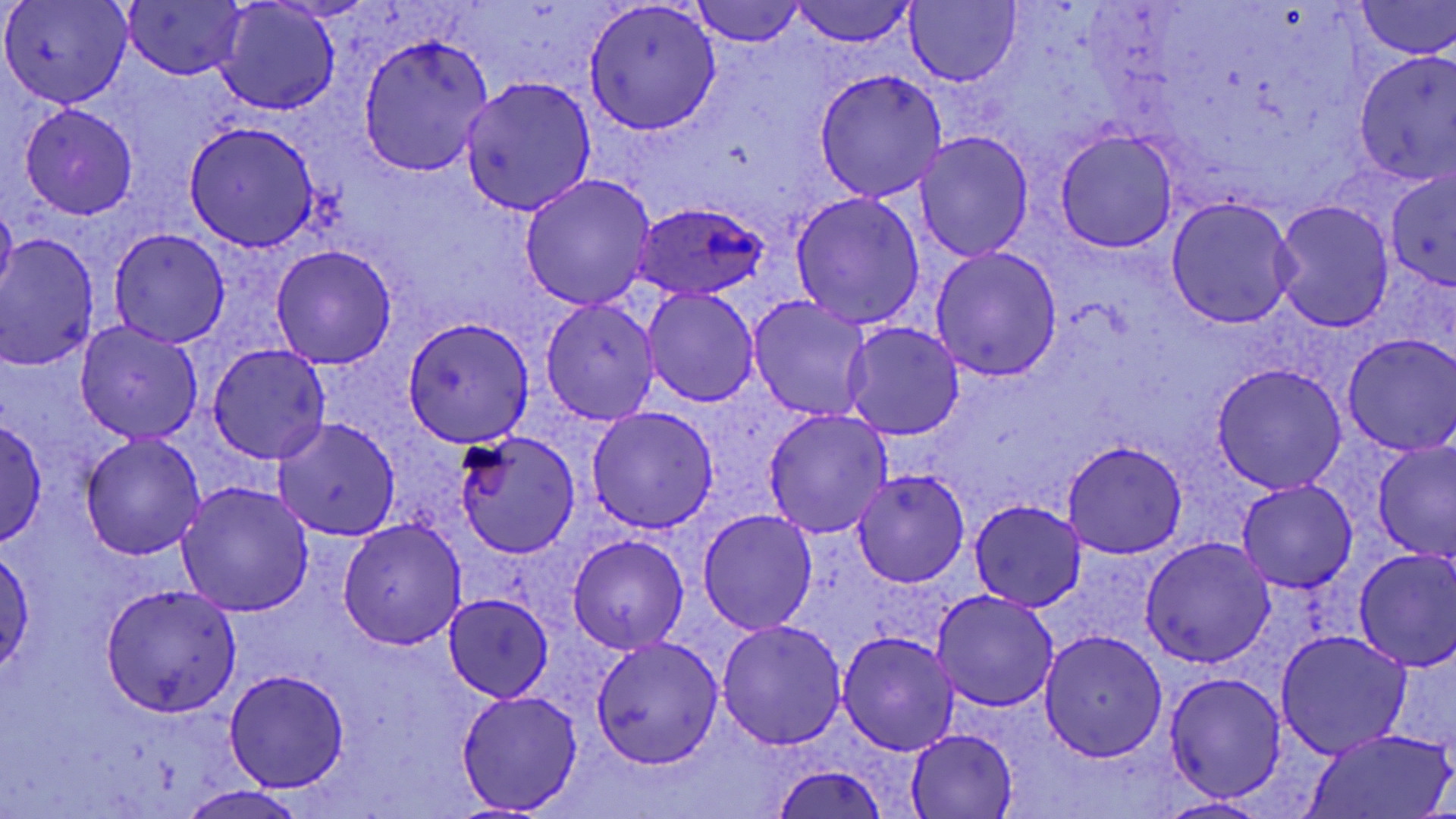

Summary:
  - Coordinate format: approximate bounding boxes as (x1, y1, x2, y2) in pixels
  - Plasmodium ovale-infected red blood cell locations: (633, 202, 768, 301)
  - Uninfected red blood cell locations: (2, 0, 133, 108), (1358, 0, 1456, 59), (693, 1, 804, 48), (124, 2, 246, 79), (217, 2, 340, 116), (584, 2, 722, 135), (790, 2, 915, 47), (906, 2, 1020, 86), (357, 33, 493, 176), (1354, 49, 1456, 185), (813, 68, 949, 200), (461, 77, 597, 217), (22, 105, 137, 218), (184, 122, 319, 250), (1054, 131, 1179, 253), (915, 133, 1033, 261), (1386, 168, 1456, 290), (520, 174, 657, 310), (790, 192, 925, 330), (0, 197, 17, 301), (1166, 197, 1297, 328), (1273, 200, 1394, 331), (108, 228, 230, 346), (0, 233, 101, 371), (271, 245, 396, 369), (930, 246, 1062, 382), (643, 288, 758, 407), (746, 297, 874, 423), (541, 299, 660, 425), (403, 318, 533, 447), (73, 322, 204, 444), (841, 323, 965, 441), (1342, 333, 1456, 455), (207, 344, 331, 464), (1212, 363, 1347, 494), (586, 406, 718, 533), (763, 409, 894, 537), (272, 416, 401, 540), (0, 417, 48, 546), (455, 431, 581, 559), (77, 432, 204, 559), (1063, 439, 1187, 558), (1373, 442, 1456, 562), (852, 469, 969, 587), (1237, 479, 1358, 593), (177, 481, 315, 618), (968, 499, 1088, 611), (1173, 500, 1317, 636), (697, 508, 818, 633), (338, 517, 467, 651), (568, 535, 688, 655), (1140, 537, 1277, 666), (0, 544, 35, 679), (1352, 548, 1456, 672), (97, 582, 243, 719), (929, 591, 1059, 713), (444, 593, 554, 702), (716, 619, 847, 750), (1038, 630, 1167, 761), (837, 631, 960, 755), (1275, 631, 1410, 757), (592, 636, 724, 769), (224, 669, 350, 791), (1165, 671, 1287, 802), (455, 689, 584, 813), (1302, 727, 1450, 819), (907, 729, 1018, 818), (770, 765, 890, 819), (176, 786, 312, 819), (1157, 796, 1267, 818)
  - Slide-level diagnosis: Plasmodium ovale
  - Field of view: one of a larger specimen
  - Modality: optical microscopy
  - Magnification: 1000x
  - Image size: 1456×819 pixels
  - Preparation: thin blood smear
  - Stain: May-Grünwald-Giemsa